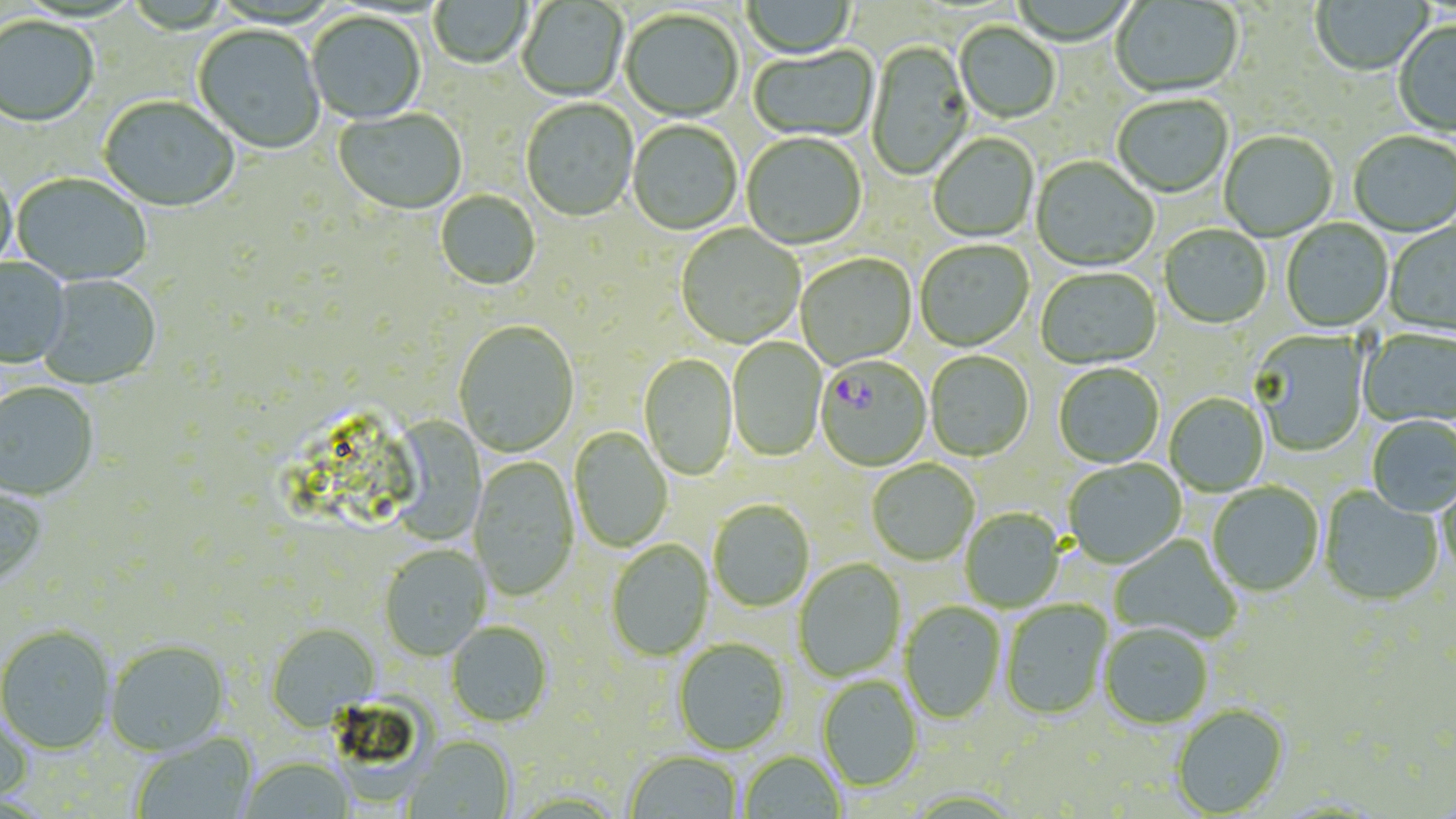 Approximate bounding boxes as (x1, y1, x2, y2) in pixels. Uninfected red blood cell locations: (428, 0, 532, 71), (742, 0, 857, 60), (1311, 0, 1434, 78), (1110, 1, 1243, 98), (517, 2, 628, 103), (620, 10, 743, 123), (307, 13, 426, 126), (0, 18, 100, 128), (955, 23, 1060, 125), (1393, 23, 1456, 136), (192, 26, 325, 155), (866, 41, 973, 182), (749, 46, 878, 143), (1112, 95, 1232, 200), (99, 97, 239, 214), (520, 100, 638, 223), (334, 110, 467, 216), (627, 121, 742, 236), (1219, 132, 1338, 242), (1348, 132, 1456, 238), (741, 134, 866, 251), (929, 134, 1039, 243), (1030, 157, 1158, 274), (0, 171, 17, 277), (11, 174, 151, 287), (435, 191, 541, 291), (1281, 219, 1393, 333), (1383, 221, 1456, 339), (675, 225, 805, 349), (1159, 225, 1272, 329), (915, 241, 1034, 352), (796, 254, 917, 370), (0, 258, 71, 369), (1036, 269, 1162, 371), (37, 274, 162, 391), (453, 321, 580, 458), (1358, 329, 1456, 429), (1249, 331, 1370, 456), (727, 337, 827, 463), (925, 351, 1033, 462), (638, 353, 738, 481), (1053, 364, 1164, 468), (0, 383, 100, 503), (1164, 393, 1269, 496), (378, 410, 493, 546), (1366, 416, 1456, 518), (569, 428, 673, 552), (469, 456, 579, 601), (1063, 459, 1186, 570), (867, 460, 980, 566), (1436, 476, 1456, 583), (1207, 483, 1324, 598), (0, 484, 49, 589), (1318, 486, 1443, 608), (708, 501, 815, 613), (960, 509, 1065, 612), (1110, 535, 1242, 644), (606, 539, 714, 662), (379, 546, 489, 661), (793, 559, 906, 682), (1000, 601, 1114, 720), (900, 602, 1006, 725), (265, 622, 380, 732), (446, 622, 553, 728), (1100, 624, 1212, 730), (0, 626, 116, 755), (674, 638, 791, 755), (106, 641, 230, 757), (817, 677, 922, 792), (1171, 705, 1290, 817), (0, 712, 35, 806), (132, 732, 258, 819), (404, 735, 515, 819), (740, 751, 846, 818), (625, 752, 743, 819), (239, 758, 354, 818). Plasmodium falciparum-infected red blood cell locations: (815, 358, 931, 472). Slide-level diagnosis: Plasmodium falciparum. One field of a larger specimen. Image is 1456×819 pixels. Optical microscopy. 1000x magnification. Thin blood film. May-Grünwald-Giemsa-stained preparation.